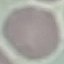 Result: no malaria parasites detected. Giemsa-stained preparation. Acquired by smartphone through the microscope eyepiece. Automatically extracted cell patch, resized to 64 × 64 pixels. Thin blood film.